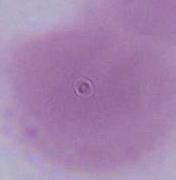
modality: micrograph
magnification: 1000x
identification: red blood cell